Classify this cell by malaria status.
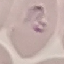
It is parasitized.

stain: Giemsa
image_type: automatically extracted cell patch, resized to 64 × 64 pixels
preparation: thin blood smear
capture: smartphone camera at the microscope eyepiece